Rate the background quality.
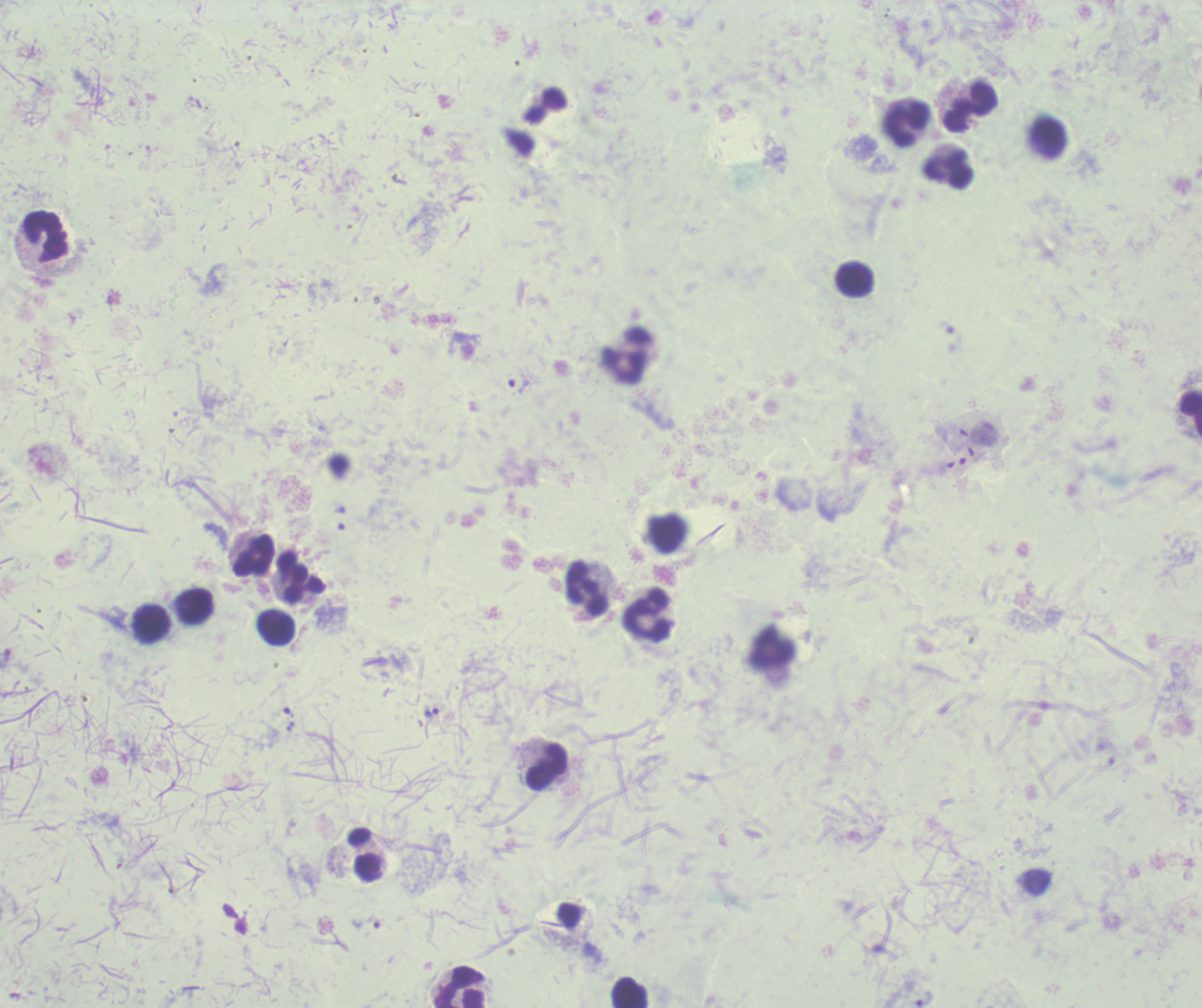

It is poor.

coordinate format = approximate centers as [x, y] in pixels
leukocyte locations = [971, 107], [905, 123], [946, 169], [48, 237], [855, 279], [626, 356], [1190, 410], [253, 555], [301, 576], [586, 588], [194, 607], [647, 615], [151, 623], [277, 628], [773, 646], [546, 767], [460, 987], [628, 991]
trophozoite locations = [518, 385], [431, 712], [366, 923], [924, 998]
image size = 1202×1008 pixels
stain = Romanowsky
field of view = one from this slide
result = malaria parasites identified
preparation = thick blood film
context = previously used in a real diagnosis
magnification = 100x